Locate platelets.
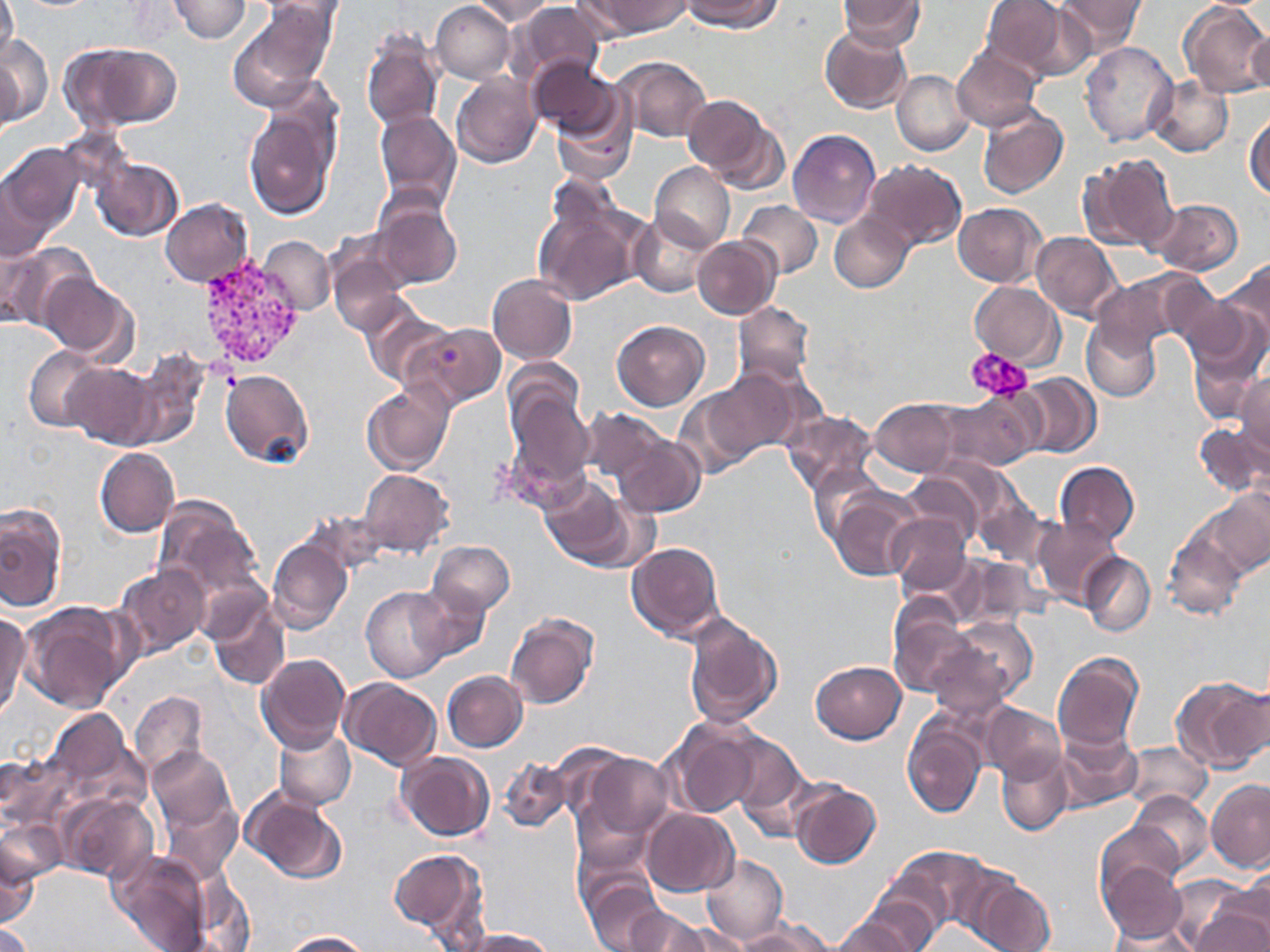

Approximate bounding boxes as (x1, y1, x2, y2) in pixels.
Platelets: (967, 347, 1033, 402).

slide_level_diagnosis: Plasmodium vivax
image_size: 1270×952 pixels
modality: optical microscopy
field_of_view: one of a larger specimen
uninfected_red_blood_cell_locations: 'approximate bounding boxes as (x1, y1, x2, y2) in pixels: (0, 0, 18, 68), (168, 0, 251, 42), (254, 0, 346, 22), (472, 0, 553, 25), (591, 0, 693, 37), (684, 0, 781, 32), (983, 0, 1076, 77), (1055, 0, 1147, 54), (1180, 0, 1270, 98), (430, 1, 515, 83), (836, 1, 926, 50), (509, 2, 605, 85), (228, 6, 334, 111), (1250, 25, 1270, 100), (818, 27, 912, 113), (358, 31, 444, 132), (0, 36, 52, 128), (1080, 41, 1177, 147), (64, 42, 183, 131), (951, 46, 1041, 132), (1, 52, 22, 140), (613, 55, 712, 141), (528, 59, 620, 141), (893, 71, 974, 156), (450, 73, 542, 169), (1147, 74, 1233, 156), (550, 87, 638, 185), (684, 96, 773, 181), (244, 102, 341, 222), (977, 105, 1069, 199), (375, 110, 461, 210), (1246, 112, 1270, 199), (704, 117, 790, 197), (789, 130, 881, 228), (0, 142, 84, 244), (1081, 153, 1178, 252), (91, 157, 183, 242), (863, 161, 967, 251), (650, 162, 734, 253), (1, 170, 56, 264), (373, 198, 462, 288), (534, 198, 642, 306), (161, 199, 254, 286), (1150, 199, 1242, 275), (737, 201, 822, 278), (953, 203, 1048, 288), (830, 212, 915, 293), (629, 213, 712, 295), (1030, 232, 1121, 322), (260, 236, 335, 315), (691, 236, 780, 320), (1, 244, 97, 334), (326, 244, 411, 336), (1219, 257, 1270, 356), (1103, 268, 1213, 350), (39, 273, 138, 362), (487, 274, 577, 366), (969, 281, 1064, 368), (359, 303, 450, 389), (732, 303, 816, 387), (1182, 307, 1268, 417), (1081, 318, 1161, 402), (613, 320, 709, 411), (406, 321, 505, 407), (24, 346, 107, 432), (122, 351, 207, 449), (58, 362, 159, 449), (219, 369, 313, 468), (699, 371, 799, 465), (1014, 373, 1101, 458), (1235, 374, 1270, 457), (362, 383, 453, 476), (504, 385, 593, 490), (937, 391, 1043, 471), (869, 400, 960, 477), (580, 407, 670, 485), (782, 409, 877, 496), (1194, 423, 1270, 498), (614, 434, 705, 518), (95, 447, 179, 537), (1055, 462, 1139, 546), (810, 464, 886, 546), (359, 469, 454, 557), (903, 470, 990, 547), (539, 477, 629, 567), (567, 489, 658, 574), (829, 489, 923, 582), (972, 491, 1052, 568), (1199, 491, 1270, 577), (153, 499, 262, 603), (0, 502, 67, 612), (884, 513, 971, 596), (1032, 516, 1120, 607), (1163, 531, 1248, 621), (267, 536, 353, 634), (428, 541, 515, 615), (626, 542, 724, 642), (1079, 552, 1155, 636), (950, 553, 1048, 628), (115, 564, 211, 659), (196, 576, 271, 650), (361, 584, 456, 683), (409, 584, 490, 663), (206, 597, 291, 690), (20, 601, 133, 714), (889, 602, 974, 696), (0, 611, 31, 718), (682, 611, 783, 729), (504, 612, 598, 709), (943, 615, 1038, 706), (926, 639, 1016, 721), (1053, 652, 1144, 752), (256, 654, 352, 754), (811, 660, 906, 743), (441, 671, 527, 752), (1173, 676, 1269, 772), (340, 679, 441, 771), (129, 690, 208, 779), (979, 703, 1065, 784), (46, 707, 134, 796), (902, 715, 989, 818), (664, 719, 763, 820), (272, 727, 355, 809), (1054, 728, 1142, 814), (724, 733, 811, 835), (1121, 740, 1211, 812), (148, 748, 235, 833), (997, 750, 1073, 834), (576, 751, 676, 843), (0, 752, 74, 832), (395, 752, 494, 841), (499, 757, 572, 833), (789, 780, 881, 868), (1205, 780, 1270, 873), (239, 788, 349, 884), (1127, 790, 1214, 877), (53, 793, 157, 884), (159, 798, 242, 884), (641, 809, 739, 896), (1, 817, 67, 887), (1096, 823, 1184, 903), (0, 834, 42, 931), (888, 846, 997, 932), (389, 847, 488, 942), (108, 849, 214, 952), (700, 853, 787, 947), (1097, 858, 1188, 944), (1220, 870, 1270, 946), (582, 874, 666, 952), (184, 875, 257, 951), (970, 876, 1056, 952), (1169, 876, 1265, 952), (857, 884, 949, 952), (625, 904, 711, 952), (834, 909, 927, 952), (1189, 910, 1270, 952), (743, 918, 836, 951), (1105, 919, 1199, 952), (0, 922, 36, 952), (657, 923, 752, 951), (462, 928, 554, 951), (279, 931, 372, 951)'
stain: May-Grünwald-Giemsa
magnification: 1000x
preparation: thin blood smear
plasmodium_vivax_infected_red_blood_cell_locations: 'approximate bounding boxes as (x1, y1, x2, y2) in pixels: (194, 253, 306, 370)'